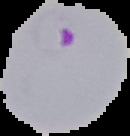
Result: malaria parasites detected. Segmented cell region on a black background. Image is 130×136 pixels. From a thin blood film.